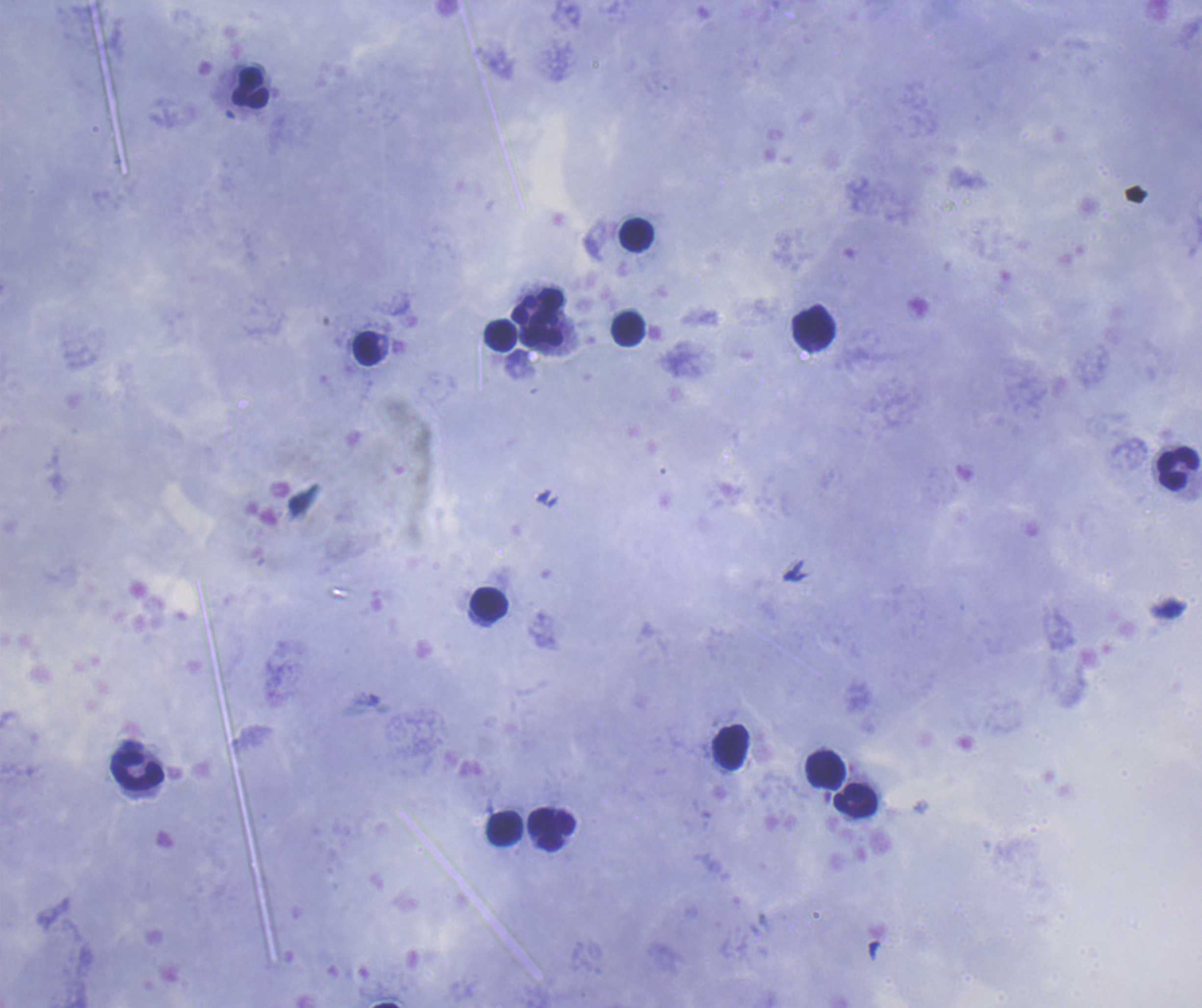 Approximate centers as {x, y} in pixels. Leukocyte locations: {249, 86}, {637, 236}, {537, 303}, {815, 326}, {628, 329}, {543, 330}, {500, 337}, {366, 347}, {1179, 469}, {490, 602}, {731, 747}, {825, 769}, {138, 770}, {856, 801}, {504, 829}, {550, 829}. Result: no malaria parasites seen. Thick smear of blood. One field from this slide. Coloration quality: good. Background quality: satisfactory. Romanowsky-stained preparation. 100x magnification. Image is 1202×1008 pixels. Previously used in a real diagnosis.